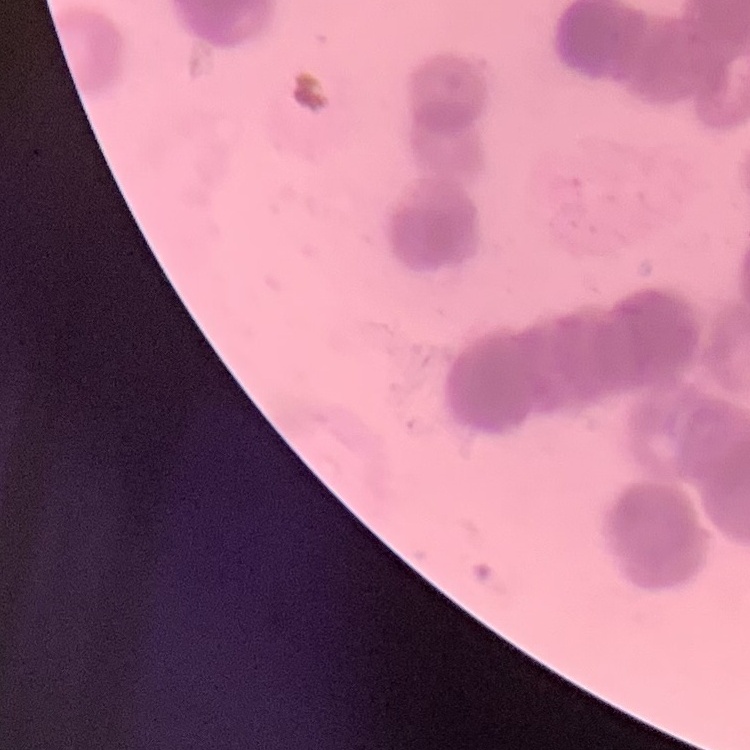

The erythrocytes exhibit rouleaux formation. Field's or Giemsa stain. One tile cut from a larger photomicrograph. Thin blood smear.